Give the position of every Plasmodium parasite visible.
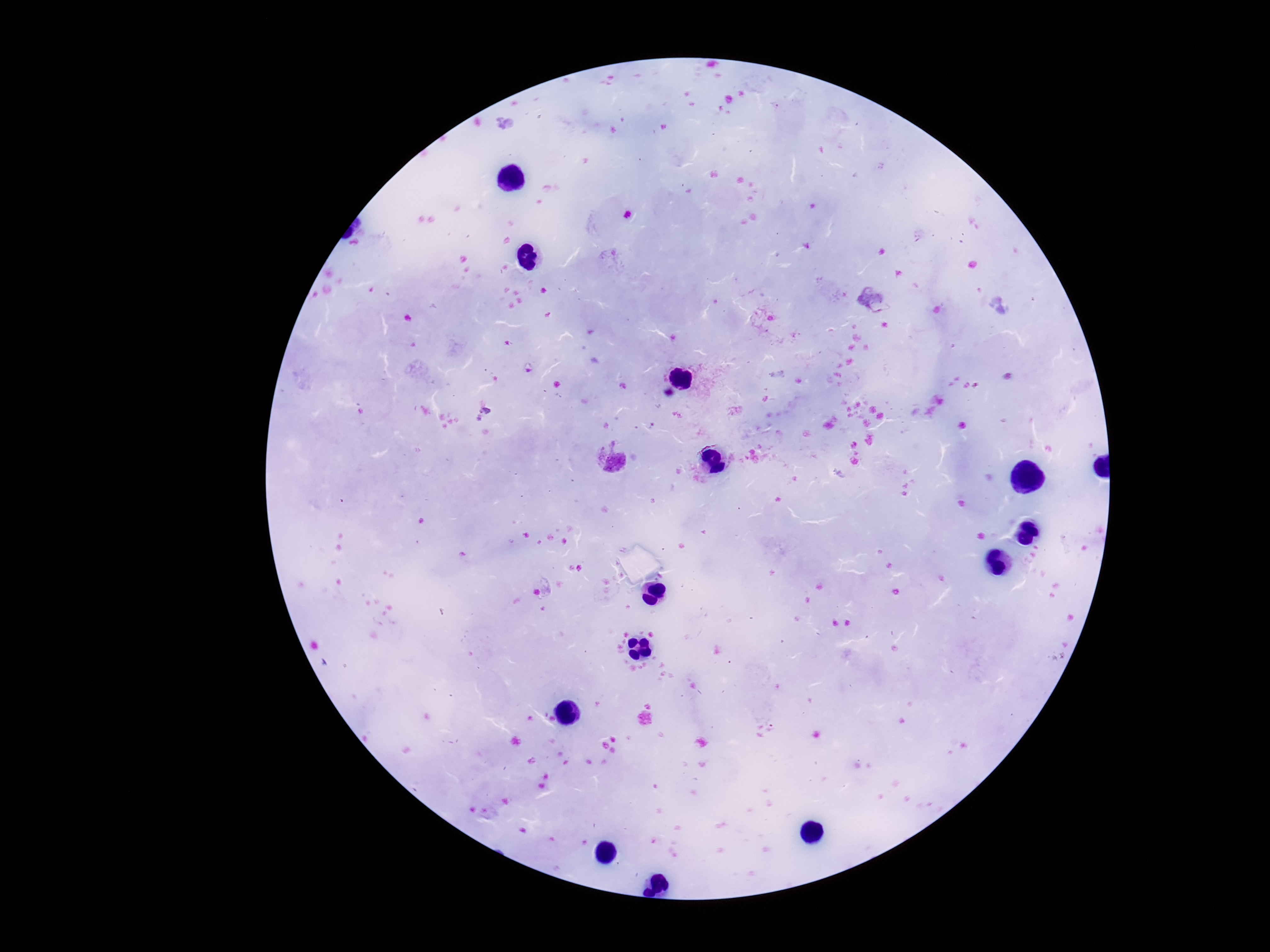
Approximate object centers, in pixels from the top-left corner.
Plasmodium parasites: (x=873, y=298), (x=485, y=417), (x=611, y=461).

capture: smartphone camera through the microscope eyepiece
image_size: 1270×952 pixels
stain: Giemsa
magnification: 100x
preparation: thick blood film
patient_malaria_status: infected
field_of_view: single